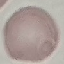
Summary:
  - Result: no malaria parasites detected
  - Stain: Giemsa
  - Image type: automatically extracted cell patch, resized to 64 × 64 pixels
  - Capture: smartphone through the microscope eyepiece
  - Preparation: thin blood smear